State which cell type is depicted.
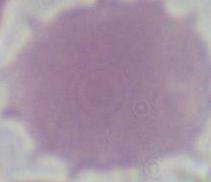
An erythrocyte.

Captured at 1000x magnification. Photomicrograph.